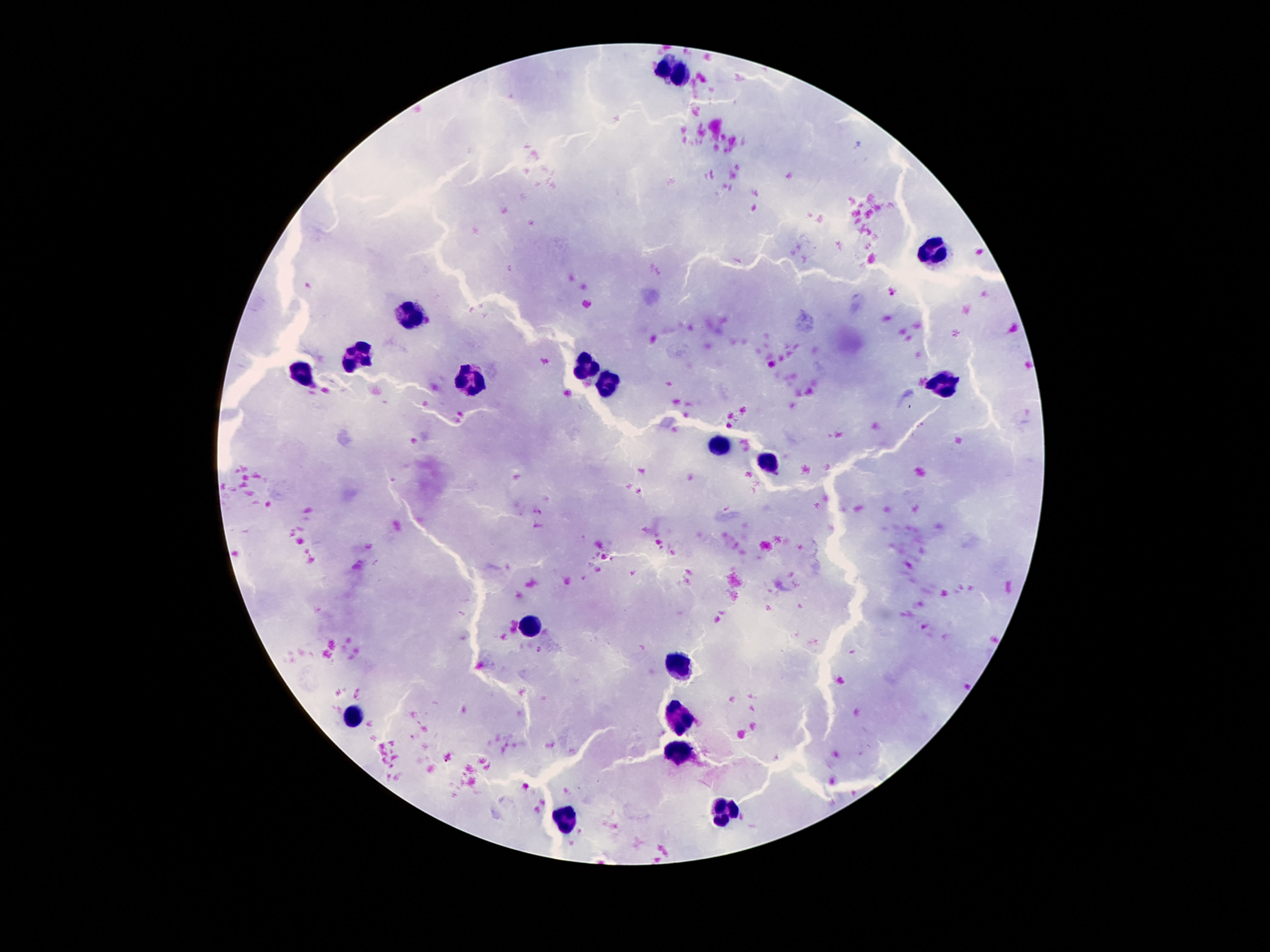
capture = smartphone camera through the microscope eyepiece
field of view = one from this slide
image size = 1270×952 pixels
leukocyte locations = approximate centers as {x, y} in pixels: {671, 69}, {938, 247}, {416, 311}, {359, 355}, {587, 370}, {301, 371}, {468, 383}, {607, 385}, {945, 388}, {720, 447}, {771, 462}, {528, 629}, {680, 667}, {682, 718}, {351, 720}, {675, 752}, {725, 808}, {566, 813}
patient malaria status = negative
preparation = thick blood smear
stain = Giemsa
magnification = 100x